Classify this cell by malaria status.
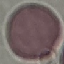

It is uninfected.

Automatically extracted cell patch, resized to 64 × 64 pixels. Acquired by smartphone through the microscope eyepiece. Thin blood film. Giemsa stain.